Describe the morphology of the erythrocytes.
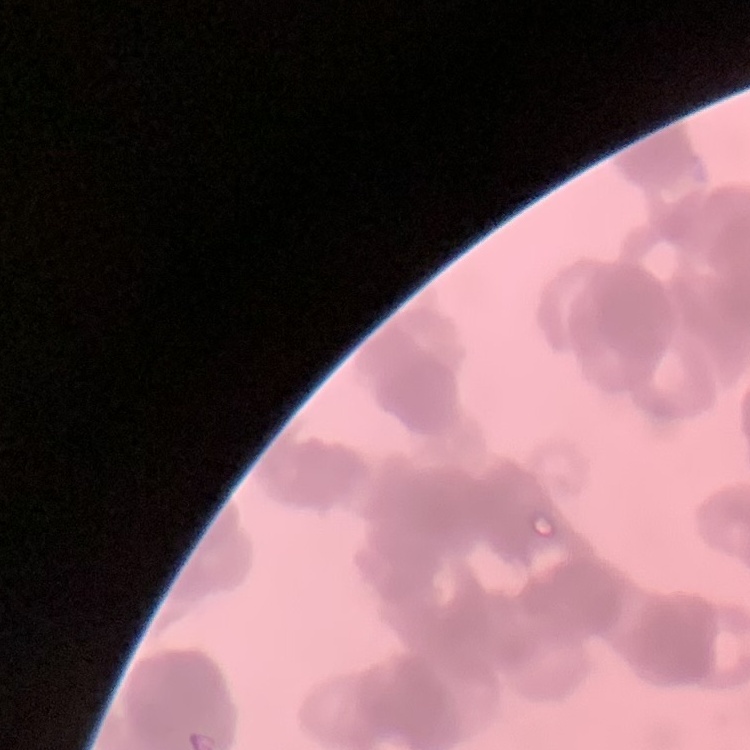
Rouleaux formation.

Thin blood film. One tile cut from a larger photomicrograph. Field's or Giemsa stain.